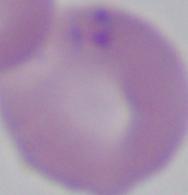
A Babesia parasite is seen. Photomicrograph. 1000x magnification.